State the blood parasite species.
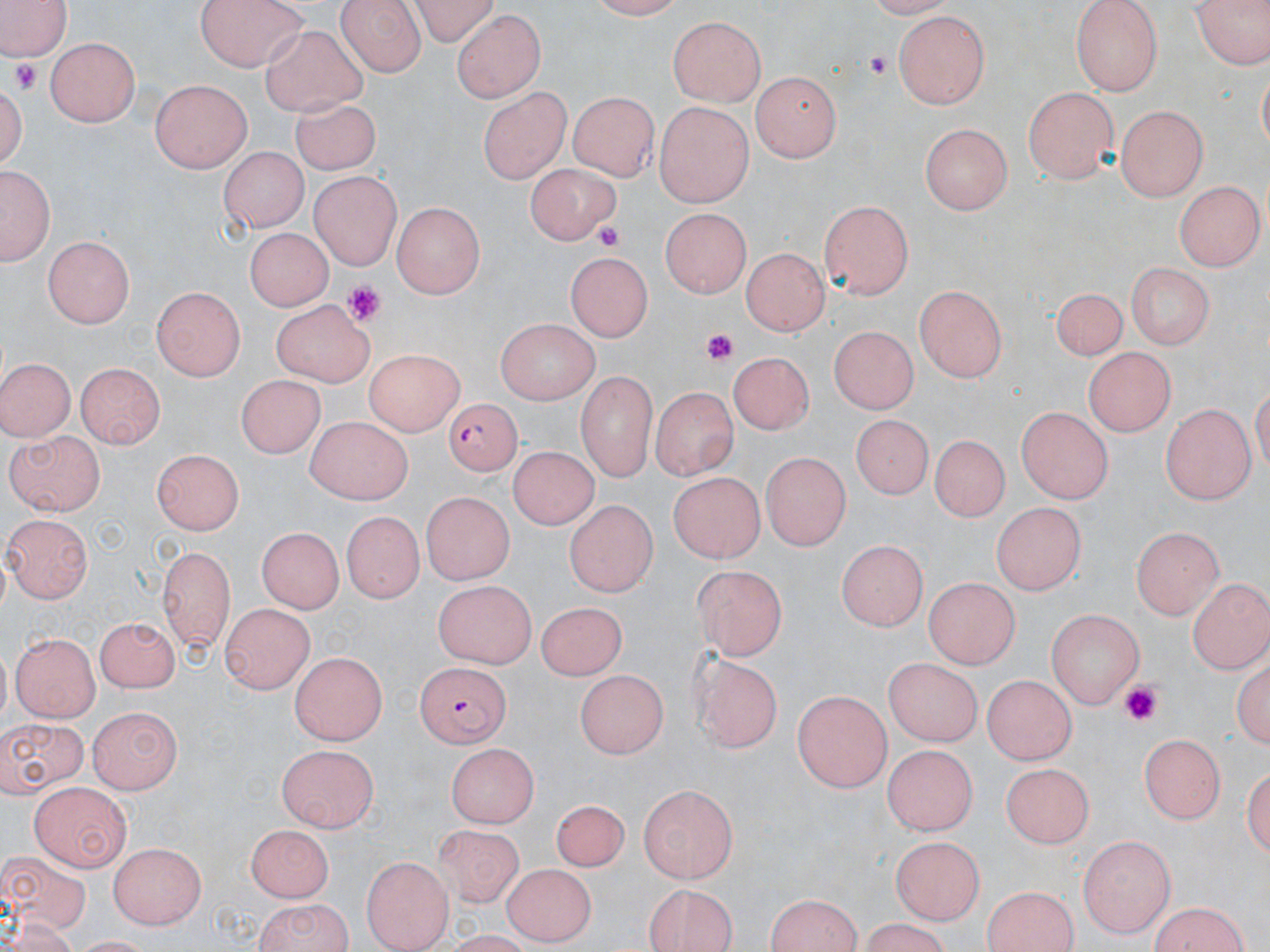

Plasmodium falciparum.

Approximate bounding boxes as [x1, y1, x2, y2] in pixels. Plasmodium falciparum-infected red blood cell locations: [440, 399, 521, 481], [412, 660, 510, 745]. Uninfected red blood cell locations: [0, 0, 76, 61], [195, 0, 307, 73], [338, 0, 428, 76], [405, 0, 500, 44], [1069, 0, 1165, 94], [1192, 0, 1266, 71], [452, 10, 543, 104], [894, 11, 990, 108], [668, 16, 767, 107], [259, 23, 366, 114], [46, 38, 142, 128], [750, 71, 842, 164], [3, 77, 30, 173], [151, 79, 254, 173], [481, 83, 571, 186], [1022, 86, 1119, 184], [569, 89, 657, 183], [291, 94, 382, 175], [654, 103, 751, 208], [1116, 103, 1210, 198], [921, 124, 1008, 215], [217, 148, 304, 237], [522, 161, 618, 246], [2, 165, 51, 267], [307, 171, 401, 269], [1176, 180, 1263, 272], [818, 199, 912, 299], [394, 200, 488, 297], [658, 210, 749, 299], [242, 228, 334, 312], [43, 234, 134, 328], [740, 247, 827, 336], [567, 254, 650, 344], [1121, 261, 1216, 349], [913, 285, 1009, 383], [1053, 287, 1122, 362], [151, 288, 244, 379], [269, 298, 370, 388], [497, 320, 597, 406], [827, 326, 921, 416], [367, 347, 464, 434], [1085, 350, 1173, 436], [729, 351, 811, 437], [0, 357, 74, 440], [74, 361, 164, 448], [235, 372, 321, 455], [576, 375, 655, 481], [649, 385, 736, 480], [1161, 403, 1257, 505], [1015, 405, 1110, 504], [852, 409, 931, 490], [301, 416, 416, 505], [2, 431, 104, 517], [934, 433, 1006, 521], [510, 447, 594, 532], [150, 449, 245, 536], [760, 452, 849, 550], [664, 471, 764, 566], [420, 493, 516, 580], [991, 500, 1083, 598], [565, 501, 653, 598], [337, 511, 425, 606], [4, 516, 95, 603], [255, 526, 343, 613], [1131, 527, 1222, 619], [837, 537, 925, 633], [238, 542, 329, 675], [156, 546, 236, 652], [688, 566, 784, 662], [921, 577, 1021, 666], [1188, 577, 1267, 674], [430, 579, 537, 669], [220, 604, 316, 695], [538, 604, 626, 681], [1046, 609, 1148, 709], [95, 613, 182, 694], [12, 632, 99, 723], [288, 652, 390, 742], [691, 652, 780, 756], [881, 663, 981, 749], [575, 671, 667, 758], [982, 674, 1077, 766], [791, 688, 893, 793], [86, 705, 178, 794], [1, 714, 85, 795], [1137, 733, 1223, 825], [882, 741, 975, 835], [448, 743, 540, 826], [278, 745, 375, 835], [1002, 762, 1094, 847], [32, 781, 131, 872], [637, 785, 737, 884], [547, 799, 629, 872], [244, 825, 336, 900], [434, 827, 525, 907], [1077, 834, 1179, 936], [889, 835, 984, 924], [109, 842, 209, 929], [0, 851, 90, 931], [360, 854, 452, 950], [504, 863, 596, 945], [981, 883, 1081, 950], [639, 885, 738, 952], [760, 892, 866, 951], [249, 897, 356, 952], [1146, 901, 1255, 952]. Platelet locations: [865, 52, 896, 82], [13, 58, 39, 93], [593, 224, 623, 250], [340, 283, 385, 325], [702, 329, 738, 367], [1120, 680, 1165, 729]. Optical microscopy. Thin blood smear. May-Grünwald-Giemsa stain. Image is 1270×952 pixels. 1000x magnification. One field of a larger specimen.